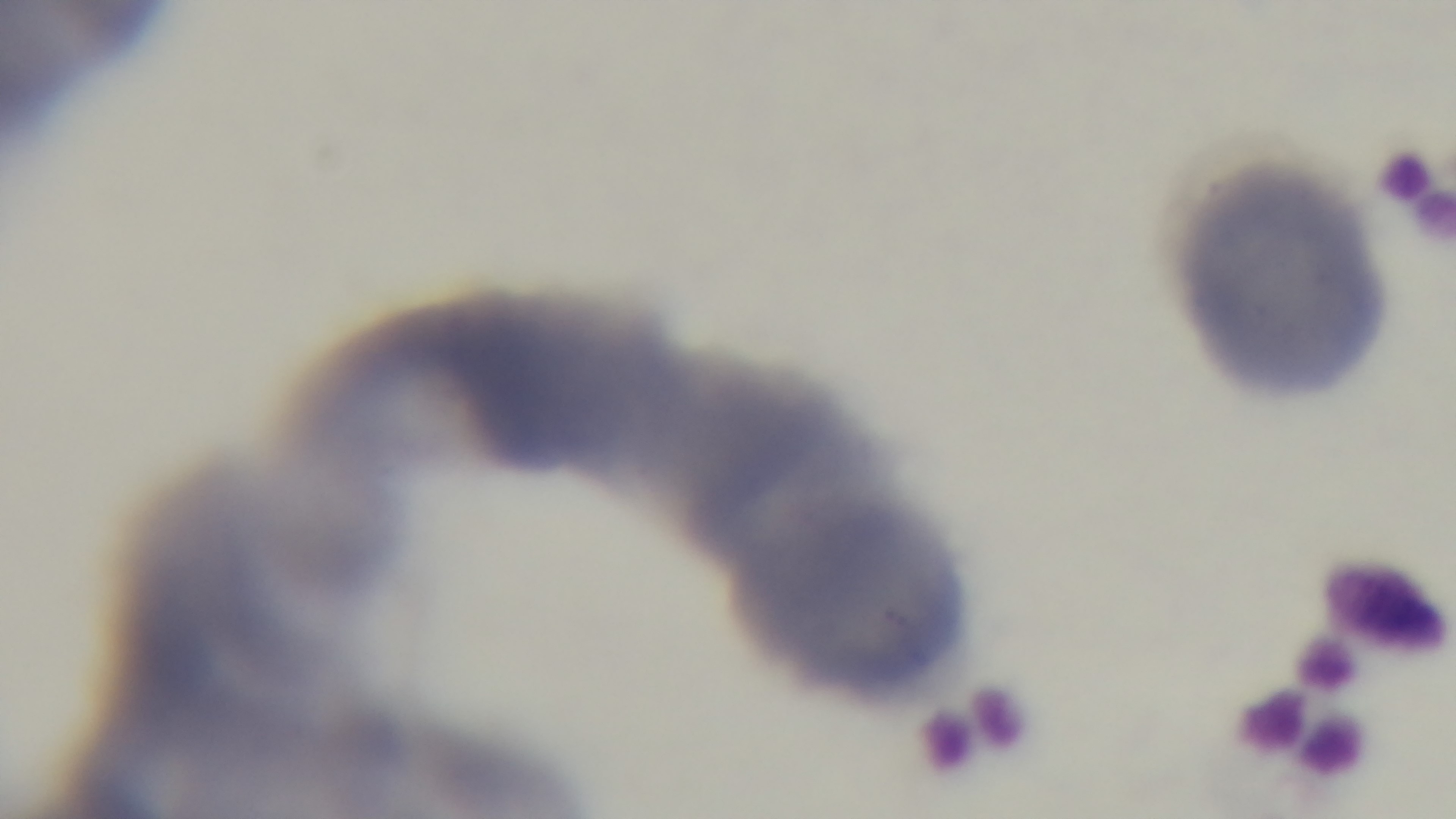
malaria status = negative
stain = Giemsa
capture = mounted 4K digital camera
field of view = one from the slide
preparation = thin smear
objective = 100x oil immersion
modality = light microscopy